Identify the blood parasite species.
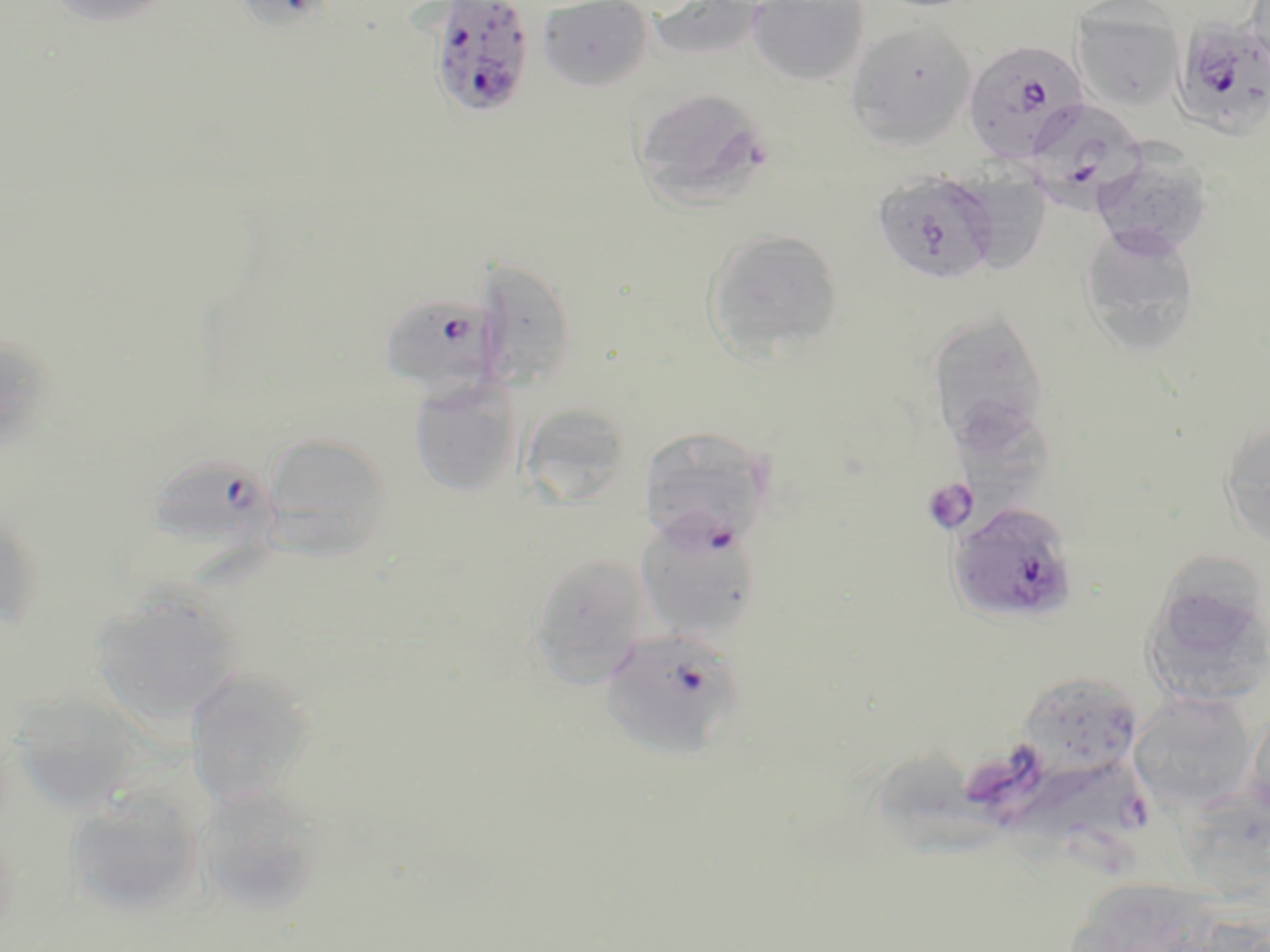

Plasmodium falciparum.

preparation = thin blood film
field of view = single
modality = optical microscopy
image size = 1270×952 pixels
stain = May-Grünwald-Giemsa
Plasmodium falciparum-infected red blood cell locations = approximate bounding boxes as (x1, y1, x2, y2) in pixels: (427, 1, 536, 121), (1171, 17, 1270, 140), (962, 39, 1089, 165), (1023, 98, 1148, 212), (872, 168, 1001, 286), (378, 291, 506, 398), (152, 454, 287, 559), (947, 500, 1081, 627), (635, 512, 764, 641), (601, 628, 745, 760)
magnification = 1000x
uninfected red blood cell locations = approximate bounding boxes as (x1, y1, x2, y2) in pixels: (45, 0, 179, 28), (231, 0, 342, 33), (538, 0, 652, 91), (645, 0, 770, 66), (865, 0, 991, 13), (747, 1, 870, 87), (1071, 3, 1184, 113), (845, 21, 975, 151), (632, 86, 773, 209), (1091, 144, 1214, 259), (956, 168, 1052, 275), (1079, 222, 1202, 356), (704, 229, 844, 359), (471, 257, 577, 390), (926, 310, 1052, 453), (0, 329, 57, 457), (409, 380, 521, 497), (960, 401, 1059, 502), (519, 403, 632, 506), (1220, 418, 1270, 550), (639, 426, 772, 547), (261, 432, 392, 556), (0, 504, 43, 632), (528, 553, 651, 688), (1142, 575, 1269, 706), (88, 589, 244, 726), (184, 666, 317, 810), (1022, 674, 1138, 769), (1128, 692, 1258, 813), (8, 695, 143, 815), (1244, 701, 1270, 828), (205, 784, 318, 916), (64, 786, 208, 919), (1062, 877, 1219, 952), (1166, 915, 1270, 952)
platelet locations = approximate bounding boxes as (x1, y1, x2, y2) in pixels: (922, 478, 977, 533)